Classify the preparation.
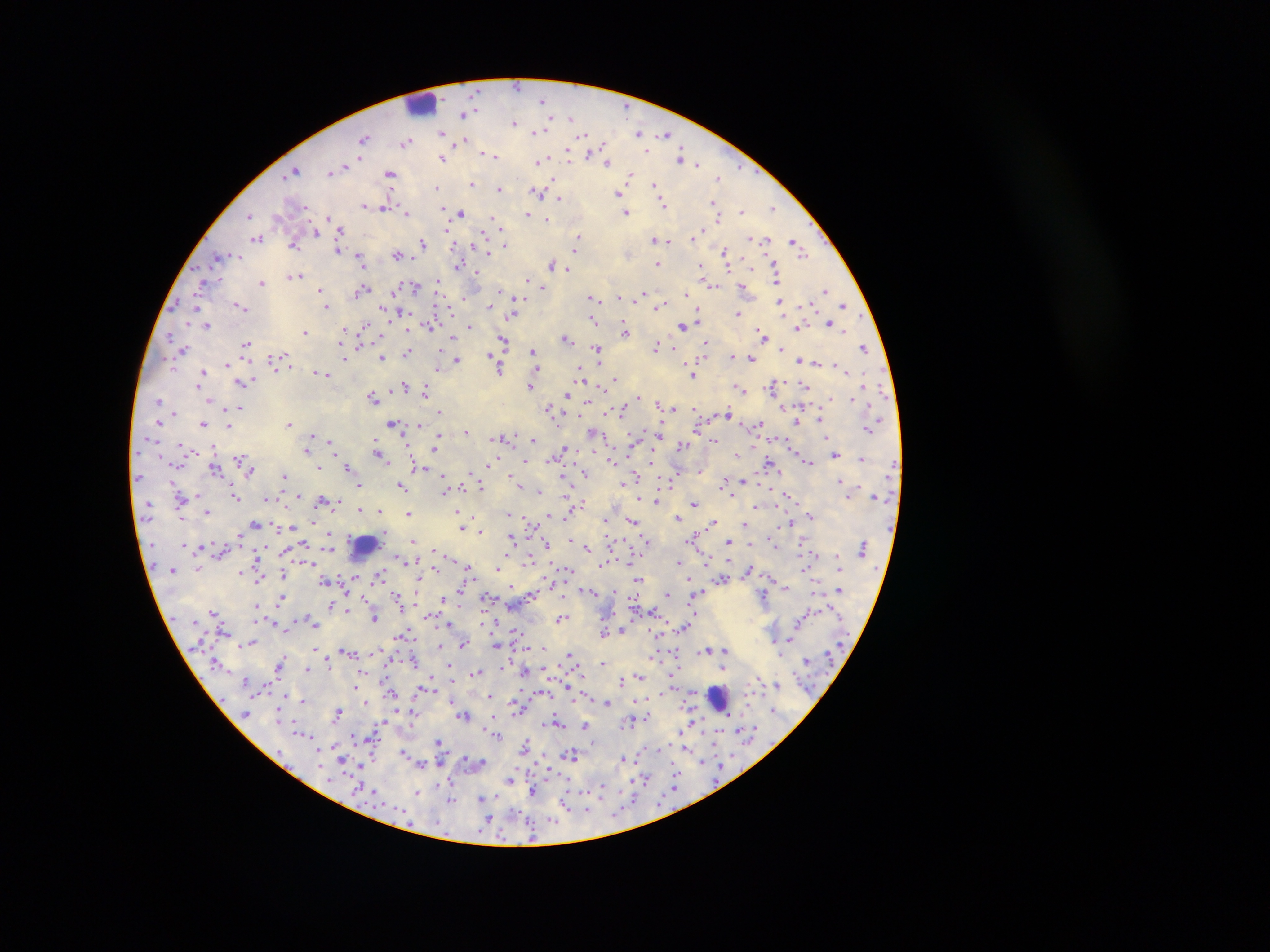

Thick blood smear.

country: Ghana
leukocyte_locations: 'approximate centers as x y in pixels: 420 104; 364 545; 718 698'
capture: mobile-phone photograph through a microscope
malaria_parasite_locations: 'approximate centers as x y in pixels: 518 85; 544 99; 464 114; 571 117; 515 122; 539 130; 442 131; 641 131; 666 135; 365 138; 463 140; 407 142; 486 152; 491 154; 568 155; 602 156; 681 157; 443 158; 538 160; 688 160; 607 161; 696 163; 296 169; 331 171; 390 174; 631 175; 719 177; 472 184; 655 186; 438 187; 499 188; 539 191; 619 192; 558 198; 713 203; 663 204; 364 205; 385 207; 773 207; 741 210; 445 211; 407 212; 627 212; 461 213; 528 214; 249 216; 718 217; 328 218; 546 219; 495 220; 339 230; 700 231; 316 232; 258 238; 578 238; 694 238; 753 238; 666 239; 655 240; 762 240; 422 242; 669 242; 505 243; 294 244; 797 244; 578 246; 338 249; 488 250; 725 252; 397 254; 237 256; 218 257; 361 260; 657 264; 553 265; 459 266; 728 266; 567 268; 703 269; 775 269; 476 274; 294 275; 777 277; 527 279; 261 282; 438 282; 708 282; 202 284; 742 286; 413 287; 321 289; 542 289; 825 289; 363 290; 687 293; 643 295; 464 296; 620 296; 592 297; 594 301; 780 301; 516 302; 241 305; 661 305; 844 305; 326 306; 447 306; 489 306; 400 312; 513 314; 738 314; 594 320; 699 321; 830 322; 206 325; 364 325; 430 325; 683 325; 470 327; 625 328; 797 328; 345 329; 305 331; 764 334; 170 336; 453 338; 566 338; 504 341; 360 342; 246 344; 705 344; 657 347; 864 347; 183 349; 597 349; 782 349; 533 351; 408 352; 491 353; 732 355; 382 357; 274 359; 750 359; 799 360; 344 361; 457 361; 816 361; 227 363; 838 364; 289 365; 499 368; 438 369; 536 369; 318 372; 202 373; 324 373; 693 374; 581 376; 615 377; 201 382; 241 382; 530 384; 772 384; 805 385; 865 385; 406 386; 425 390; 741 390; 567 394; 373 397; 210 398; 638 398; 830 399; 853 399; 159 401; 586 401; 658 402; 664 404; 239 407; 782 407; 673 408; 696 409; 551 411; 622 411; 441 412; 727 414; 820 420; 797 421; 160 422; 289 422; 393 423; 203 424; 418 424; 228 425; 758 425; 867 429; 661 430; 465 431; 593 432; 313 434; 506 438; 534 439; 828 439; 636 440; 330 441; 714 441; 379 444; 683 444; 435 447; 307 448; 190 449; 566 449; 835 454; 240 455; 381 455; 736 456; 494 458; 861 458; 527 460; 612 461; 808 461; 320 467; 348 467; 214 468; 418 468; 701 469; 428 471; 251 472; 585 473; 443 474; 284 475; 564 476; 637 478; 744 480; 839 480; 725 481; 444 484; 480 484; 401 485; 624 485; 360 486; 519 486; 403 488; 537 490; 733 494; 298 495; 847 495; 197 496; 237 496; 266 497; 790 497; 656 500; 324 501; 338 501; 584 502; 694 503; 757 506; 360 510; 208 511; 379 511; 457 511; 408 512; 510 513; 549 515; 811 515; 679 518; 180 519; 608 520; 633 520; 312 521; 527 521; 714 521; 789 523; 256 524; 745 525; 292 526; 463 527; 481 530; 241 535; 329 536; 512 536; 694 537; 647 540; 414 541; 730 541; 546 544; 750 544; 304 545; 187 546; 586 546; 432 550; 258 556; 707 557; 632 558; 528 560; 406 561; 678 561; 467 567; 806 567; 434 568; 498 568; 566 569; 749 570; 242 573; 283 574; 380 575; 355 576; 259 578; 639 579; 723 579; 551 582; 786 588; 417 589; 590 590; 699 591; 838 591; 667 593; 531 594; 398 595; 764 596; 282 597; 365 597; 443 598; 489 599; 399 603; 332 605; 257 606; 653 611; 214 612; 695 613; 430 616; 375 618; 311 619; 561 619; 692 619; 272 622; 485 622; 451 623; 314 624; 685 627; 291 629; 624 630; 514 632; 604 632; 404 636; 790 639; 251 643; 463 643; 497 645; 440 646; 539 646; 314 648; 343 649; 709 649; 725 650; 350 652; 569 655; 655 655; 281 661; 329 661; 805 661; 603 662; 510 663; 449 664; 726 665; 280 666; 306 669; 526 669; 477 671; 364 672; 639 677; 621 681; 354 684; 426 685; 569 685; 421 688; 544 692; 392 693; 286 694; 489 695; 304 701; 451 701; 606 701; 366 702; 517 708; 409 710; 774 710; 412 711; 339 712; 463 715; 647 717; 631 719; 383 722; 557 722; 696 723; 585 724; 744 729; 494 731; 681 731; 302 733; 496 734; 354 736; 440 741; 593 742; 525 745; 684 747; 659 748; 404 751; 572 754; 624 757; 343 759; 468 759; 423 762; 704 762; 361 763; 675 772; 511 779; 646 779; 442 782; 602 788; 376 789; 675 789; 418 791; 533 791; 600 792; 494 795; 482 797; 451 800; 565 804; 586 810; 488 818; 533 836'
field_of_view: single
image_size: 1270×952 pixels